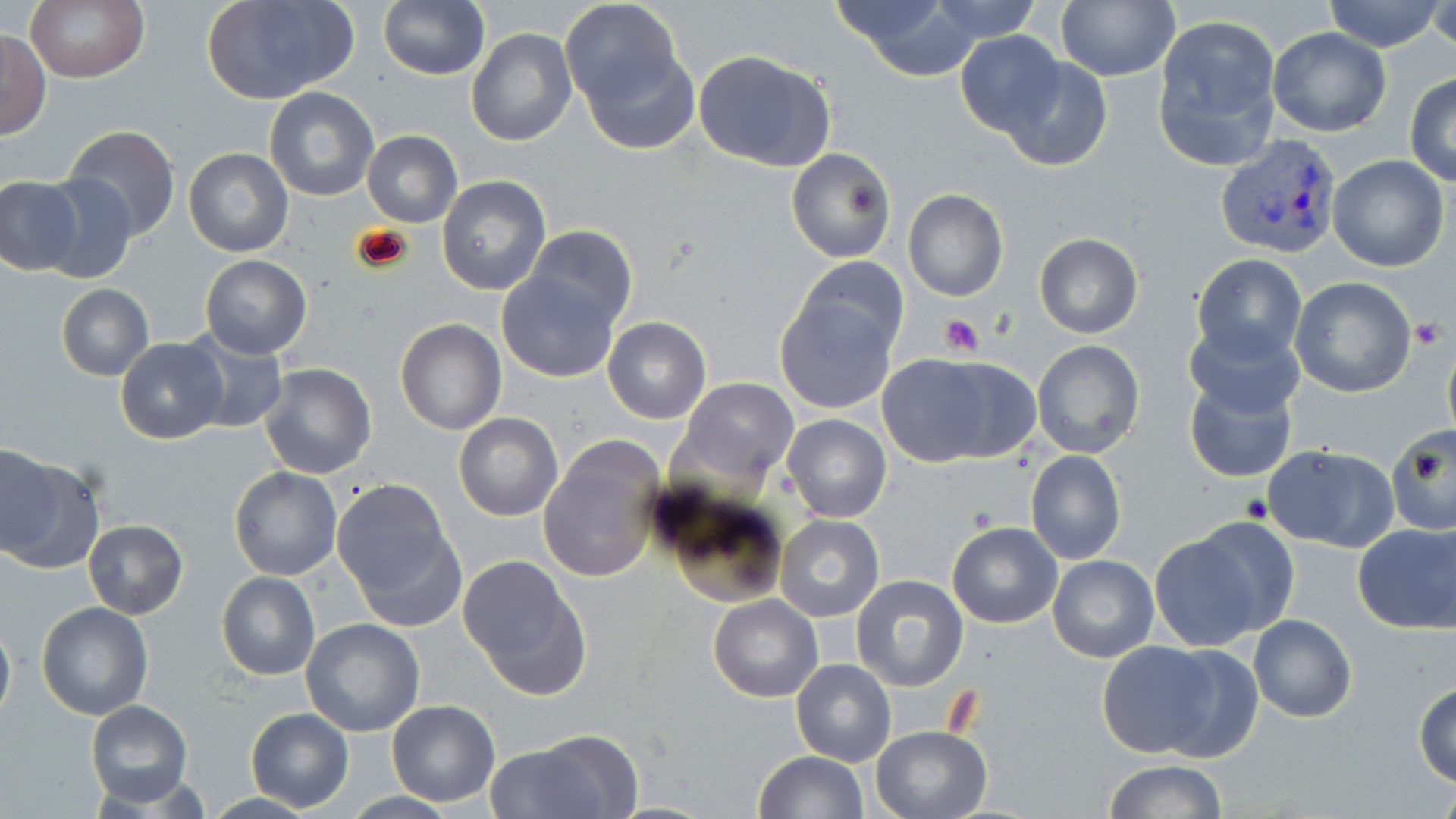

Summary:
  - Coordinate format: approximate bounding boxes as named x1/y1/x2/y2 corners in pixels
  - Plasmodium vivax-infected red blood cell locations: (x1=1213, y1=133, x2=1346, y2=261)
  - Platelet locations: (x1=938, y1=314, x2=984, y2=357), (x1=1411, y1=316, x2=1447, y2=349), (x1=1242, y1=493, x2=1275, y2=522)
  - Uninfected red blood cell locations: (x1=204, y1=0, x2=356, y2=106), (x1=377, y1=0, x2=489, y2=80), (x1=560, y1=0, x2=683, y2=110), (x1=828, y1=0, x2=985, y2=78), (x1=929, y1=0, x2=1043, y2=43), (x1=1056, y1=0, x2=1179, y2=82), (x1=1320, y1=0, x2=1447, y2=51), (x1=26, y1=1, x2=148, y2=83), (x1=1425, y1=2, x2=1455, y2=60), (x1=1152, y1=17, x2=1282, y2=166), (x1=1266, y1=27, x2=1391, y2=135), (x1=1, y1=29, x2=50, y2=139), (x1=465, y1=29, x2=578, y2=147), (x1=955, y1=32, x2=1067, y2=137), (x1=582, y1=46, x2=700, y2=155), (x1=693, y1=50, x2=837, y2=172), (x1=1000, y1=57, x2=1112, y2=172), (x1=1405, y1=72, x2=1456, y2=186), (x1=264, y1=86, x2=378, y2=201), (x1=60, y1=125, x2=180, y2=242), (x1=361, y1=129, x2=463, y2=229), (x1=786, y1=146, x2=895, y2=263), (x1=184, y1=148, x2=293, y2=258), (x1=1327, y1=155, x2=1450, y2=272), (x1=37, y1=171, x2=137, y2=284), (x1=438, y1=175, x2=552, y2=295), (x1=0, y1=176, x2=83, y2=276), (x1=902, y1=189, x2=1007, y2=302), (x1=523, y1=225, x2=639, y2=329), (x1=1034, y1=234, x2=1142, y2=338), (x1=1190, y1=252, x2=1307, y2=366), (x1=795, y1=254, x2=908, y2=360), (x1=200, y1=255, x2=311, y2=358), (x1=496, y1=268, x2=621, y2=383), (x1=1288, y1=276, x2=1418, y2=397), (x1=57, y1=284, x2=154, y2=380), (x1=774, y1=299, x2=897, y2=413), (x1=603, y1=317, x2=711, y2=423), (x1=1182, y1=317, x2=1307, y2=421), (x1=395, y1=319, x2=506, y2=435), (x1=180, y1=330, x2=286, y2=436), (x1=116, y1=338, x2=228, y2=444), (x1=1031, y1=340, x2=1146, y2=460), (x1=884, y1=352, x2=1038, y2=462), (x1=259, y1=363, x2=376, y2=478), (x1=1182, y1=373, x2=1299, y2=484), (x1=680, y1=378, x2=799, y2=482), (x1=454, y1=413, x2=562, y2=521), (x1=782, y1=413, x2=891, y2=523), (x1=1386, y1=427, x2=1455, y2=537), (x1=539, y1=439, x2=664, y2=584), (x1=1262, y1=444, x2=1398, y2=553), (x1=1, y1=446, x2=55, y2=554), (x1=1026, y1=449, x2=1127, y2=565), (x1=0, y1=452, x2=104, y2=576), (x1=230, y1=467, x2=342, y2=581), (x1=332, y1=480, x2=462, y2=625), (x1=661, y1=491, x2=790, y2=608), (x1=776, y1=514, x2=884, y2=621), (x1=82, y1=519, x2=187, y2=620), (x1=1352, y1=521, x2=1455, y2=635), (x1=947, y1=522, x2=1062, y2=629), (x1=1147, y1=526, x2=1277, y2=652), (x1=1047, y1=555, x2=1159, y2=662), (x1=458, y1=557, x2=590, y2=698), (x1=217, y1=572, x2=320, y2=680), (x1=849, y1=573, x2=970, y2=693), (x1=708, y1=594, x2=822, y2=703), (x1=37, y1=602, x2=154, y2=720), (x1=1248, y1=614, x2=1358, y2=723), (x1=0, y1=617, x2=15, y2=727), (x1=299, y1=619, x2=425, y2=737), (x1=1097, y1=640, x2=1220, y2=758), (x1=1147, y1=642, x2=1264, y2=763), (x1=791, y1=659, x2=895, y2=766), (x1=1414, y1=680, x2=1456, y2=787), (x1=386, y1=699, x2=499, y2=805), (x1=86, y1=700, x2=193, y2=807), (x1=247, y1=709, x2=353, y2=812), (x1=870, y1=726, x2=991, y2=819), (x1=481, y1=737, x2=633, y2=817), (x1=753, y1=750, x2=869, y2=818), (x1=1103, y1=760, x2=1229, y2=817), (x1=342, y1=791, x2=458, y2=818), (x1=198, y1=793, x2=321, y2=819)
  - Slide-level diagnosis: Plasmodium vivax
  - Preparation: thin blood smear
  - Modality: light microscopy
  - Image size: 1456×819 pixels
  - Magnification: 1000x
  - Field of view: single
  - Stain: May-Grünwald-Giemsa